Locate every leukocyte (white blood cell).
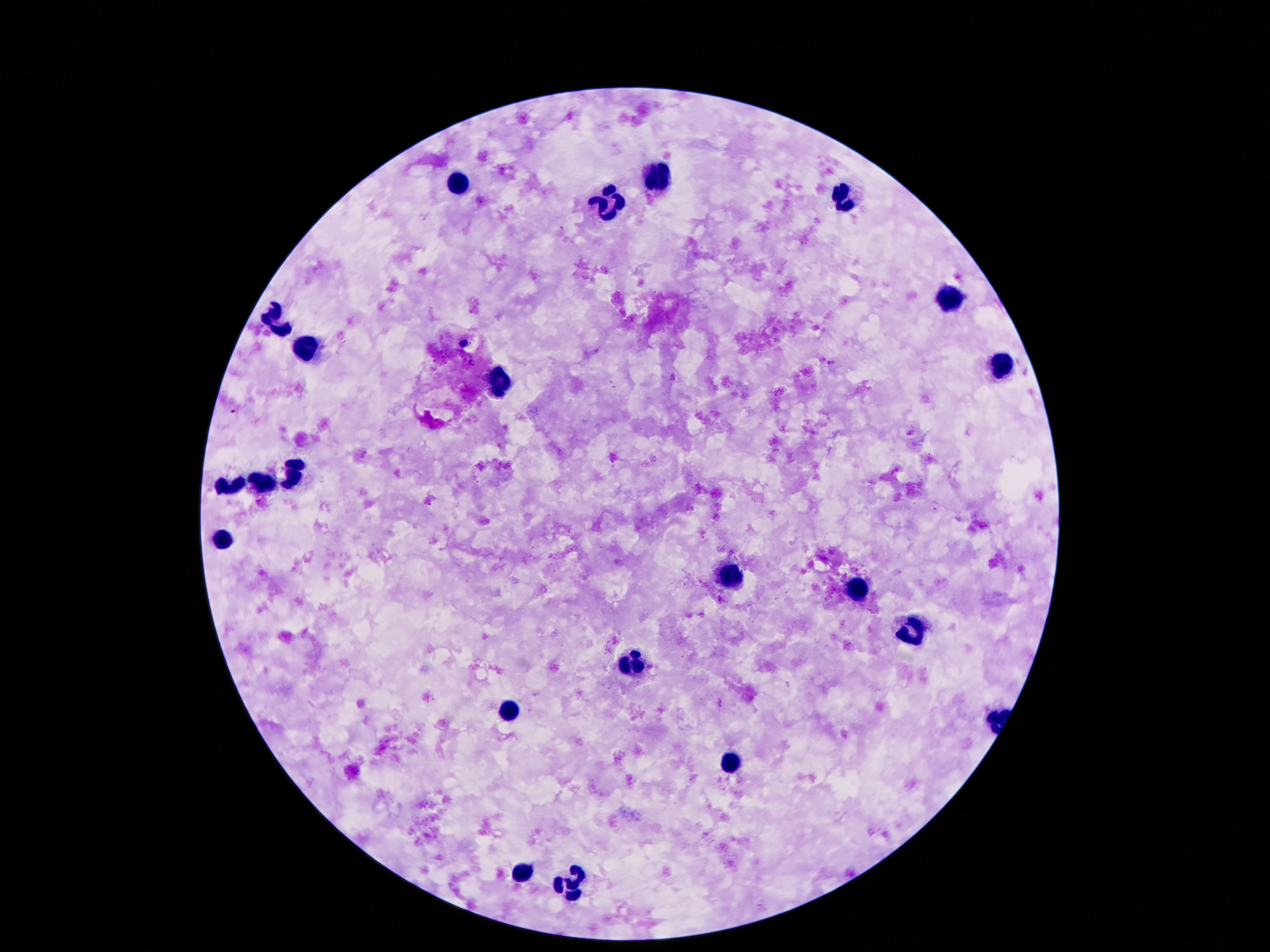

Approximate centers as {x, y} in pixels.
Leukocytes: {659, 179}, {460, 180}, {845, 194}, {610, 206}, {948, 298}, {276, 321}, {306, 351}, {999, 365}, {500, 384}, {295, 473}, {262, 482}, {227, 486}, {220, 538}, {731, 578}, {855, 592}, {918, 631}, {638, 666}, {509, 712}, {731, 762}, {521, 872}, {568, 884}.

capture = smartphone camera through the microscope eyepiece
patient malaria status = not infected
preparation = thick blood film
image size = 1270×952 pixels
magnification = 100x
stain = Giemsa
field of view = single